Report the malaria status of this cell.
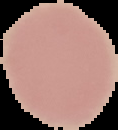

It is uninfected.

The area outside the segmented cell region is set to black. From a thin blood film. Image is 118×130 pixels.